Outline each Babesia divergens-infected red blood cell.
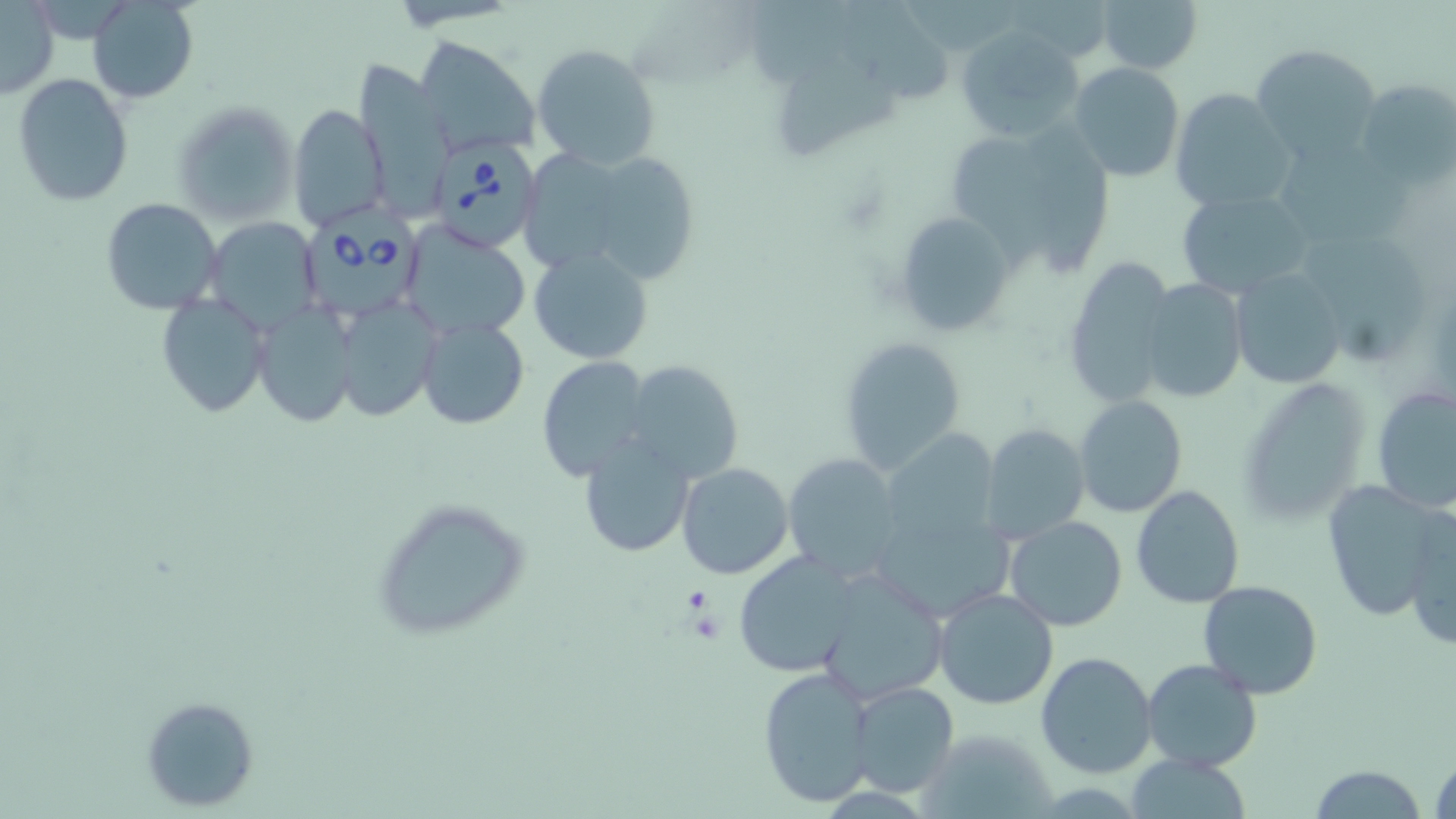

Approximate bounding boxes as named x1/y1/x2/y2 corners in pixels.
Babesia divergens-infected red blood cells: (x1=433, y1=139, x2=543, y2=252), (x1=307, y1=207, x2=427, y2=317).

slide-level diagnosis = Babesia divergens
magnification = 1000x
preparation = thin blood film
platelet locations = approximate bounding boxes as named x1/y1/x2/y2 corners in pixels: (x1=680, y1=587, x2=713, y2=618)
uninfected red blood cell locations = approximate bounding boxes as named x1/y1/x2/y2 corners in pixels: (x1=87, y1=0, x2=198, y2=103), (x1=1096, y1=0, x2=1203, y2=75), (x1=837, y1=1, x2=961, y2=106), (x1=0, y1=2, x2=58, y2=100), (x1=949, y1=24, x2=1084, y2=143), (x1=414, y1=35, x2=542, y2=156), (x1=531, y1=41, x2=663, y2=170), (x1=1250, y1=42, x2=1384, y2=164), (x1=784, y1=54, x2=904, y2=159), (x1=351, y1=57, x2=456, y2=207), (x1=1067, y1=62, x2=1185, y2=183), (x1=11, y1=73, x2=135, y2=207), (x1=1356, y1=77, x2=1453, y2=189), (x1=1168, y1=87, x2=1297, y2=214), (x1=174, y1=100, x2=299, y2=227), (x1=287, y1=103, x2=388, y2=231), (x1=961, y1=118, x2=1060, y2=265), (x1=1038, y1=130, x2=1117, y2=279), (x1=598, y1=143, x2=705, y2=287), (x1=527, y1=144, x2=623, y2=268), (x1=1283, y1=150, x2=1428, y2=263), (x1=1174, y1=188, x2=1316, y2=300), (x1=101, y1=198, x2=223, y2=316), (x1=891, y1=211, x2=1019, y2=337), (x1=205, y1=217, x2=323, y2=336), (x1=399, y1=223, x2=531, y2=342), (x1=529, y1=245, x2=655, y2=364), (x1=1307, y1=245, x2=1428, y2=365), (x1=1062, y1=255, x2=1176, y2=404), (x1=1229, y1=267, x2=1347, y2=388), (x1=1138, y1=278, x2=1247, y2=404), (x1=154, y1=292, x2=270, y2=420), (x1=333, y1=299, x2=441, y2=418), (x1=254, y1=303, x2=358, y2=426), (x1=416, y1=317, x2=531, y2=430), (x1=839, y1=335, x2=967, y2=475), (x1=536, y1=357, x2=650, y2=481), (x1=623, y1=360, x2=743, y2=482), (x1=1236, y1=377, x2=1371, y2=524), (x1=1372, y1=385, x2=1456, y2=516), (x1=1075, y1=395, x2=1187, y2=518), (x1=981, y1=423, x2=1090, y2=542), (x1=879, y1=432, x2=999, y2=549), (x1=576, y1=434, x2=697, y2=558), (x1=781, y1=452, x2=905, y2=580), (x1=677, y1=463, x2=795, y2=581), (x1=1322, y1=478, x2=1447, y2=621), (x1=1131, y1=484, x2=1246, y2=608), (x1=371, y1=496, x2=531, y2=643), (x1=868, y1=506, x2=1013, y2=624), (x1=1402, y1=508, x2=1455, y2=652), (x1=1003, y1=516, x2=1129, y2=633), (x1=732, y1=550, x2=862, y2=678), (x1=812, y1=567, x2=951, y2=705), (x1=1197, y1=580, x2=1326, y2=700), (x1=931, y1=587, x2=1060, y2=710), (x1=1035, y1=651, x2=1159, y2=778), (x1=1140, y1=658, x2=1264, y2=773), (x1=757, y1=666, x2=875, y2=807), (x1=849, y1=681, x2=960, y2=799), (x1=141, y1=697, x2=258, y2=812), (x1=1430, y1=748, x2=1455, y2=819), (x1=1125, y1=755, x2=1255, y2=817), (x1=1306, y1=765, x2=1428, y2=818)
modality = light microscopy
stain = May-Grünwald-Giemsa
image size = 1456×819 pixels
field of view = single